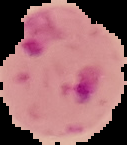

{
  "image_size": "127×145 pixels",
  "preparation": "thin blood smear",
  "image_type": "segmented cell region on a black background",
  "result": "malaria parasites detected"
}